Report the malaria status.
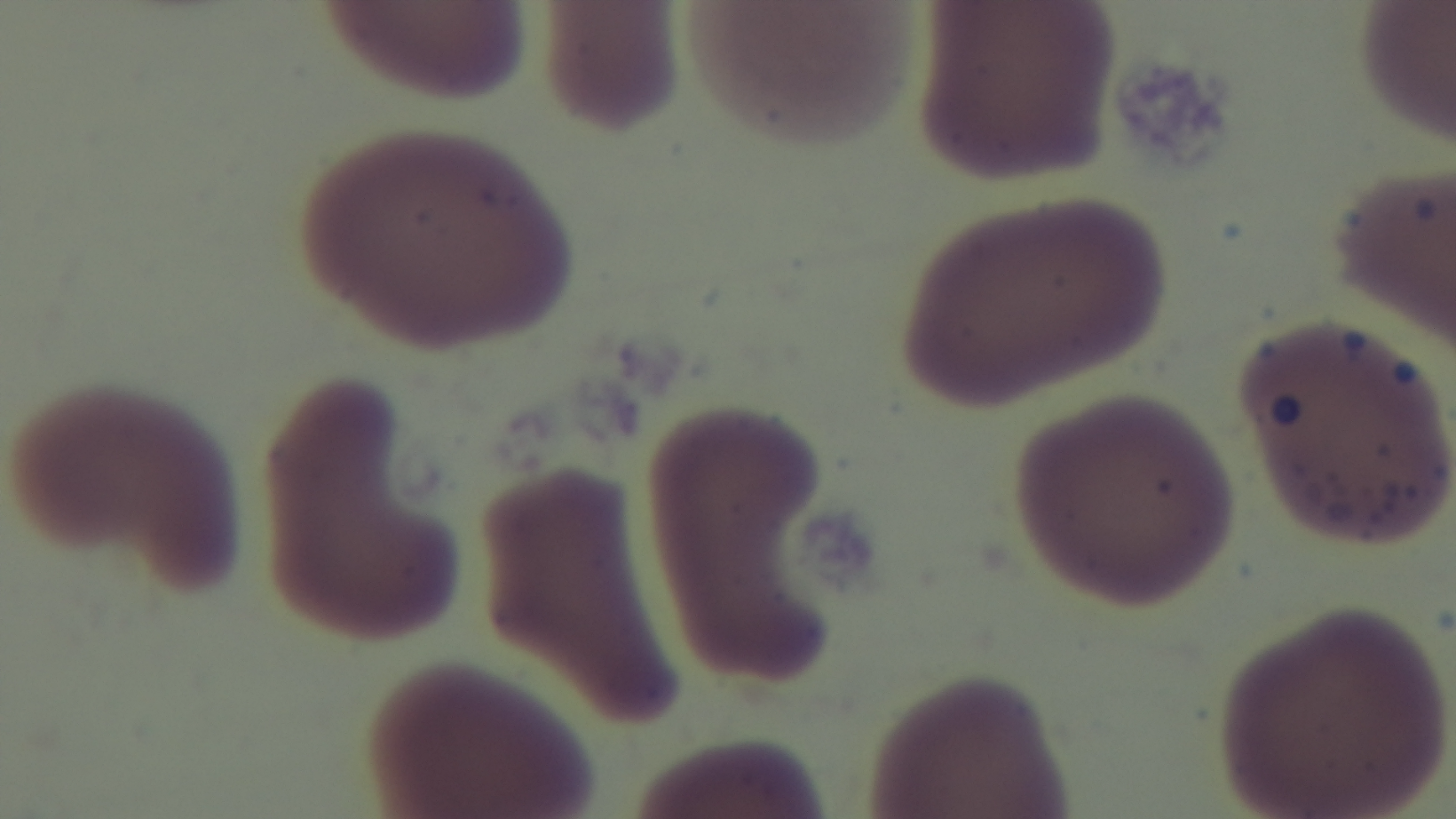

It is uninfected.

stain = Giemsa
modality = light microscopy
preparation = thin
field of view = single
objective = 100x oil immersion
capture = mounted 4K digital camera